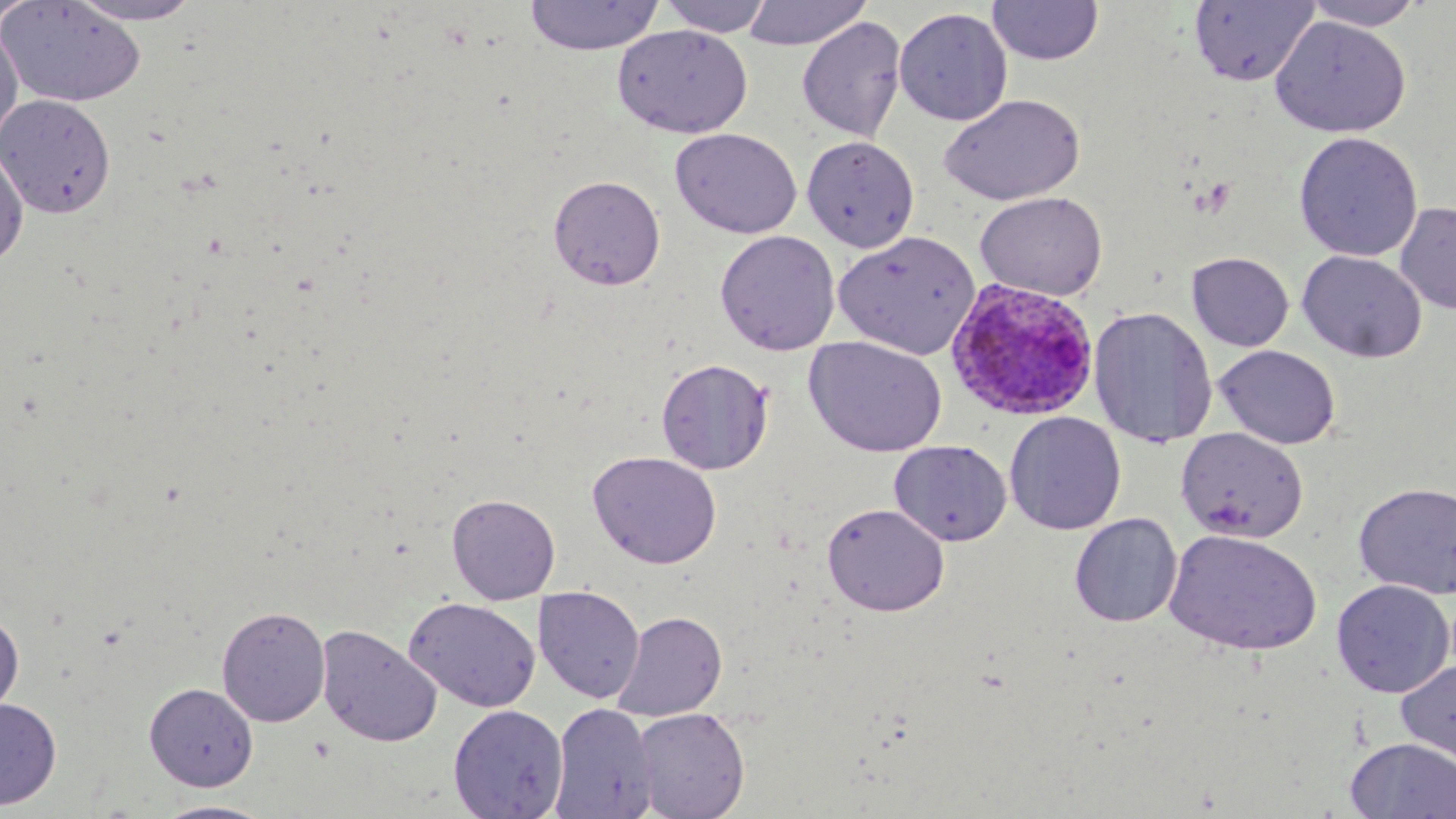
Approximate bounding boxes as [x1, y1, x2, y2] in pixels. Uninfected red blood cell locations: [65, 0, 207, 25], [524, 0, 664, 55], [656, 0, 775, 37], [742, 0, 873, 50], [1300, 0, 1427, 31], [0, 1, 147, 108], [1, 1, 39, 29], [986, 1, 1104, 65], [1188, 1, 1321, 88], [894, 7, 1013, 126], [797, 15, 907, 143], [1270, 16, 1411, 138], [0, 22, 24, 153], [612, 25, 753, 138], [940, 93, 1086, 205], [0, 94, 116, 218], [671, 128, 802, 239], [1293, 131, 1423, 262], [802, 136, 919, 252], [0, 146, 29, 269], [548, 175, 666, 290], [975, 191, 1107, 300], [1395, 201, 1456, 316], [715, 230, 841, 355], [833, 230, 980, 359], [1297, 250, 1427, 363], [1187, 252, 1294, 351], [1087, 304, 1216, 450], [804, 336, 947, 457], [1212, 344, 1341, 450], [656, 358, 773, 475], [1004, 411, 1126, 535], [1175, 427, 1309, 543], [889, 440, 1012, 546], [587, 451, 723, 569], [1353, 481, 1456, 599], [447, 493, 560, 604], [822, 502, 950, 617], [1069, 512, 1183, 627], [1164, 528, 1322, 656], [1331, 579, 1455, 698], [533, 586, 645, 703], [404, 596, 542, 712], [216, 606, 330, 726], [0, 610, 24, 721], [611, 611, 727, 721], [316, 624, 442, 747], [1395, 659, 1456, 770], [144, 682, 258, 791], [0, 697, 62, 809], [549, 702, 658, 819], [448, 704, 568, 818], [633, 708, 750, 818], [1344, 737, 1456, 818], [150, 800, 278, 818]. Plasmodium ovale-infected red blood cell locations: [945, 279, 1101, 420]. Slide-level diagnosis: Plasmodium ovale. Single field of view. Light microscopy. Image is 1456×819 pixels. Thin blood smear. May-Grünwald-Giemsa-stained preparation. 1000x magnification.